Classify this cell by malaria status.
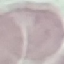

Uninfected.

preparation = thin blood film
image type = cell patch, automatically extracted from a larger field of view and resized to 64 × 64 pixels
capture = smartphone camera at the microscope eyepiece
stain = Giemsa